Assess this cell for malaria.
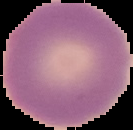

It is uninfected.

From a thin blood smear. The area outside the segmented cell region is set to black. Image is 133×130 pixels.